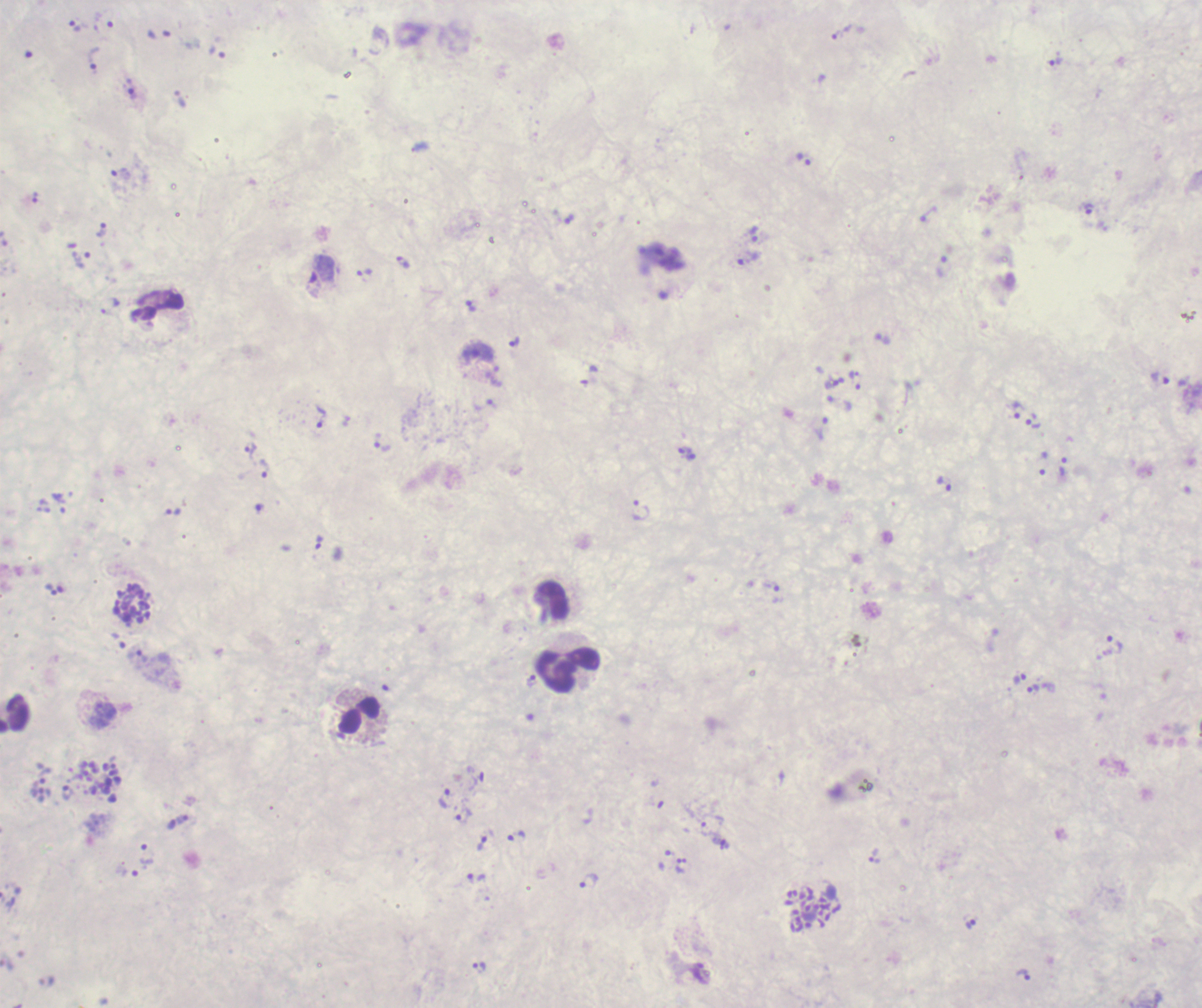
Approximate centers as (x, y) in pixels.
Summary:
  - Trophozoite locations: (75, 26), (837, 34), (94, 59), (1055, 60), (133, 94), (804, 159), (121, 173), (1089, 209), (570, 219), (102, 229), (754, 234), (82, 259), (749, 259), (403, 261), (320, 273), (364, 275), (471, 306), (514, 342), (1161, 379), (856, 381), (839, 403), (1018, 409), (320, 416), (1033, 421), (822, 429), (383, 446), (250, 450), (687, 454), (1063, 466), (264, 468), (943, 484), (173, 511), (640, 511), (319, 542), (52, 590), (1115, 644), (1019, 678), (531, 681), (1033, 689), (68, 792), (446, 798), (463, 815), (706, 828), (515, 834), (481, 843), (147, 854), (874, 856), (476, 877), (589, 882), (971, 924), (480, 968), (1023, 974)
  - Schizont locations: (132, 604), (100, 781), (813, 911)
  - Leukocyte locations: (553, 600), (568, 672), (360, 716)
  - Life-cycle stages observed: trophozoite, schizont
  - Background quality: unsatisfactory
  - Context: previously used in a real diagnosis
  - Preparation: thick blood smear
  - Result: Plasmodium parasites identified
  - Magnification: 100x
  - Field of view: single
  - Image size: 1202×1008 pixels
  - Coloration quality: bad
  - Stain: Romanowsky